Assess this cell for malaria.
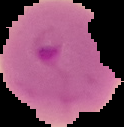

It is parasitized.

image type = segmented cell region with the area outside set to black
image size = 124×127 pixels
preparation = thin blood film